Report the malaria status of this cell.
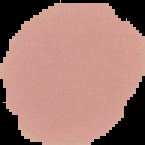
It is uninfected.

image size = 145×145 pixels
preparation = thin blood smear
image type = cell region segmented out of the field of view; surrounding area masked to black